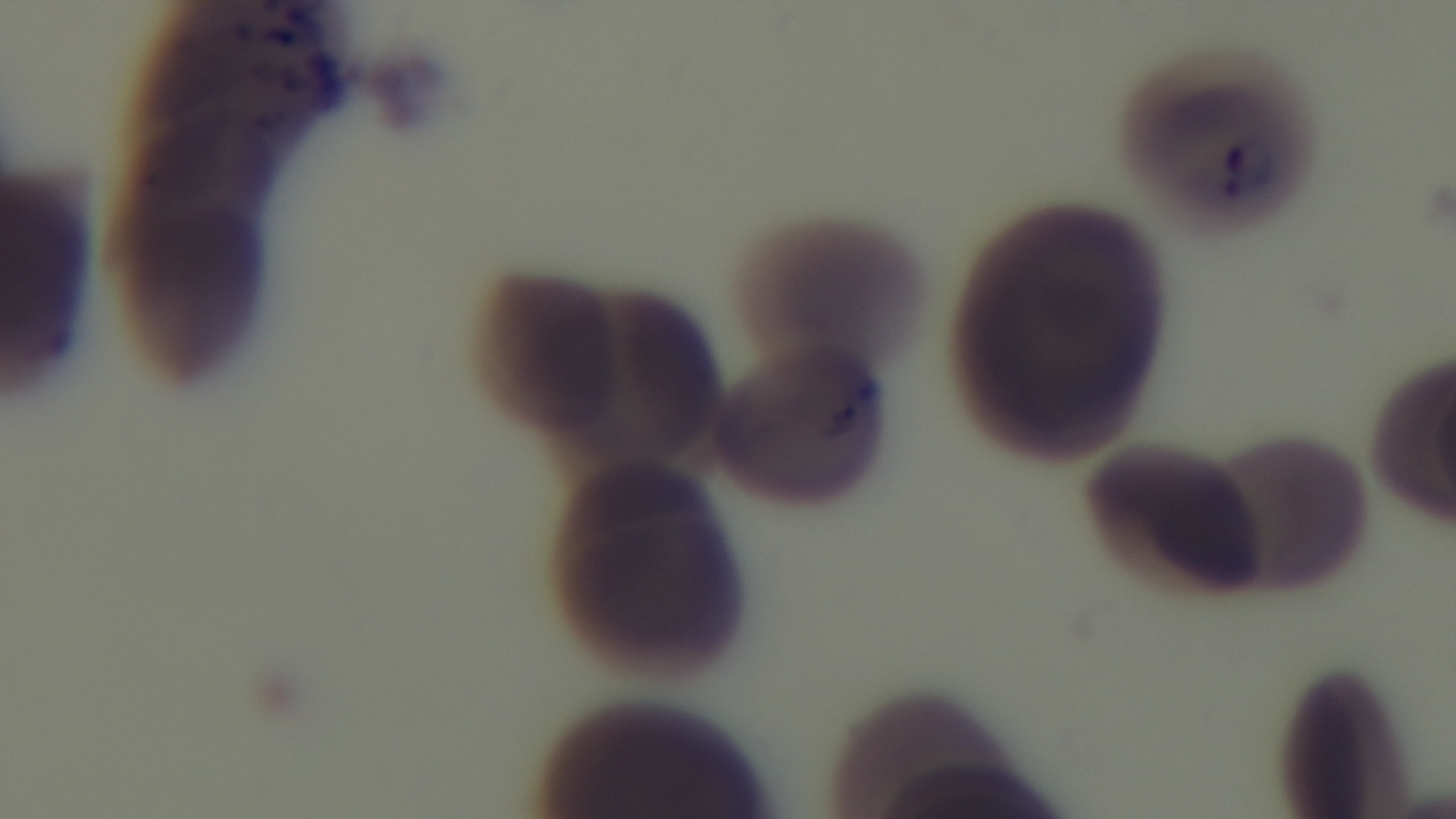

Malaria status: positive. Giemsa stain. Light microscopy. 100x oil-immersion objective. Mounted 4K digital camera. Preparation: thin blood film. Single field of view.